Identify the preparation type.
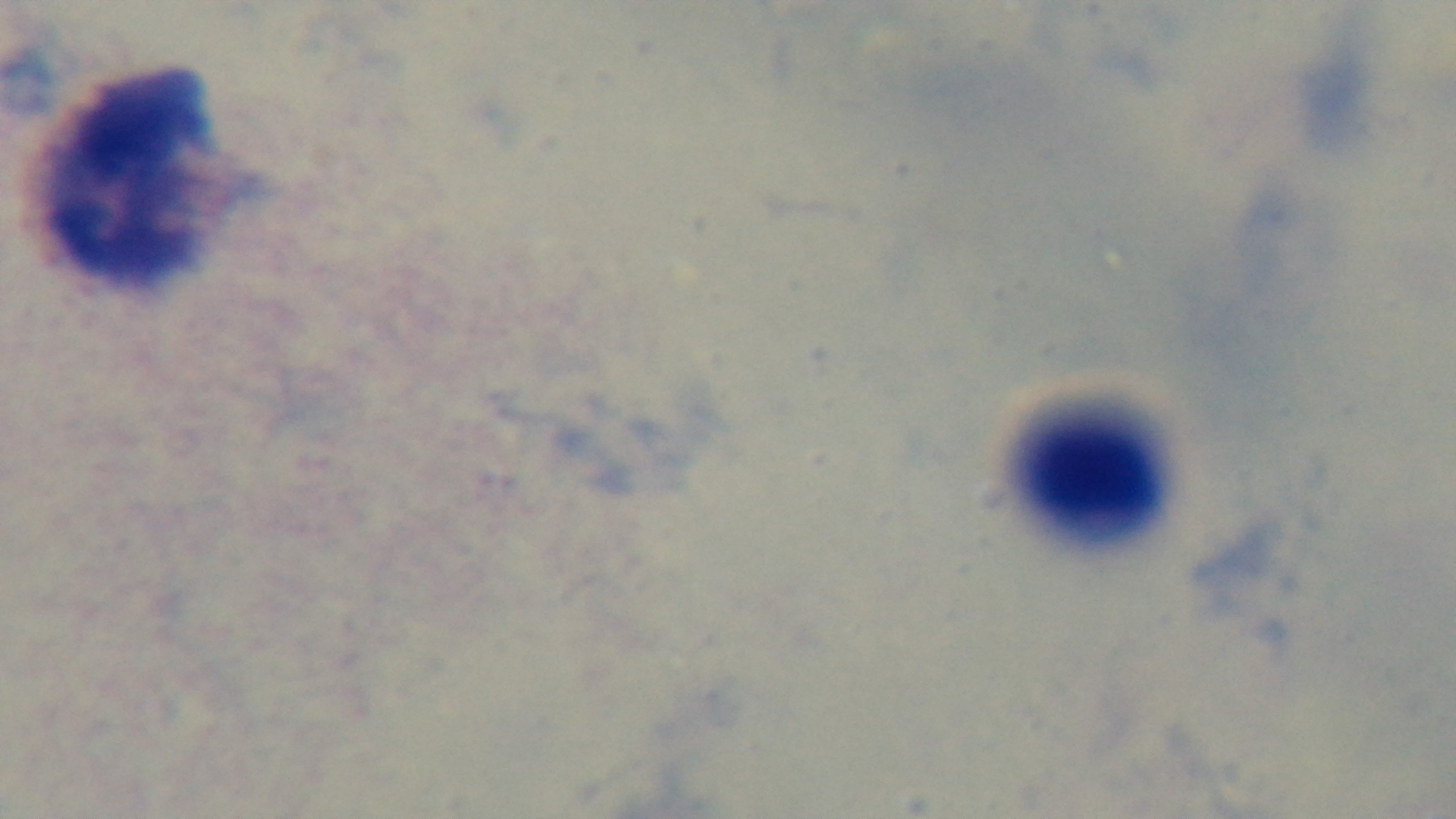
It is a thick blood film.

modality: light microscopy
stain: Giemsa
objective: 100x oil immersion
malaria_status: negative
field_of_view: single
capture: mounted 4K digital camera